Name the blood parasite species.
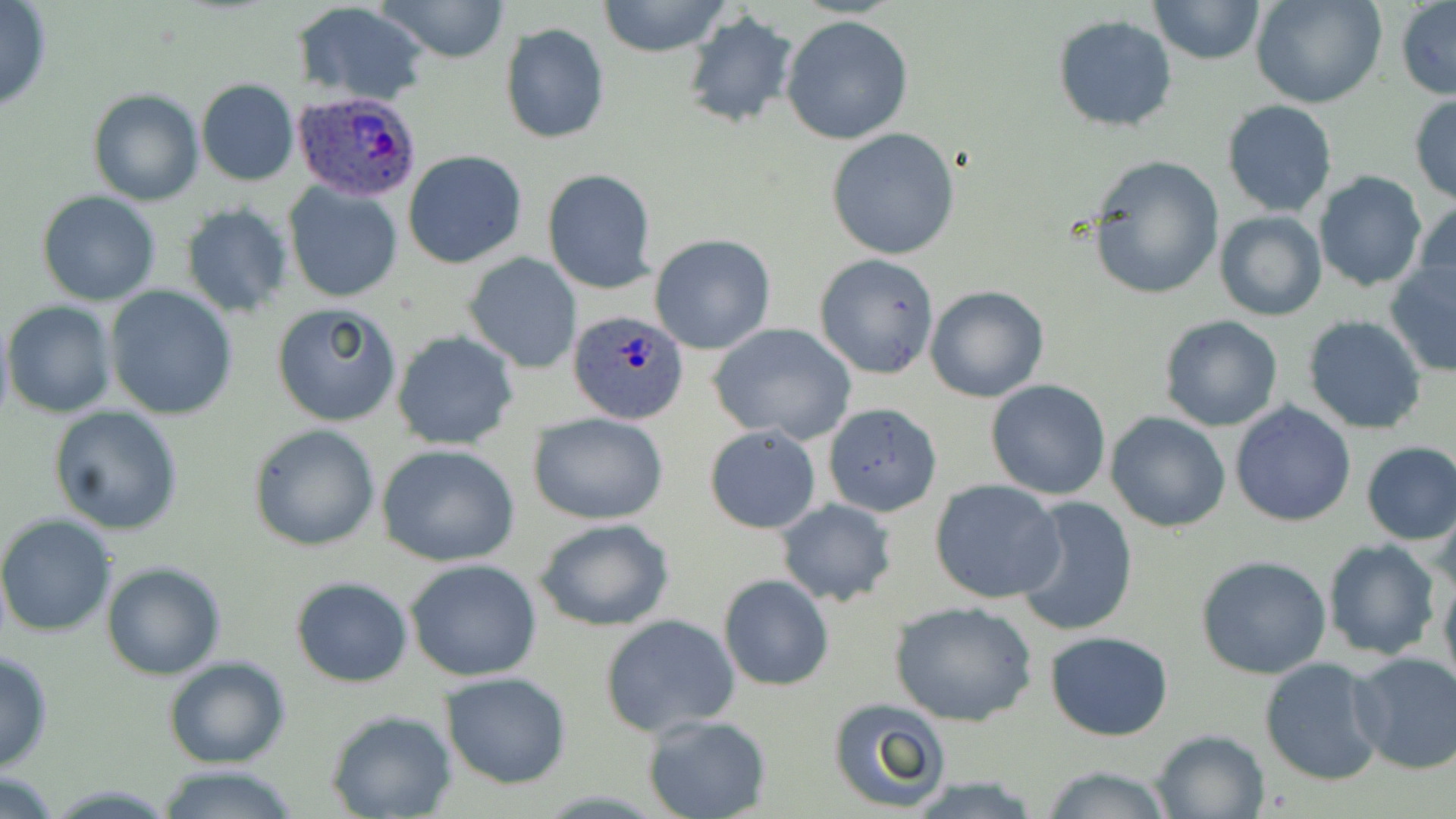

Plasmodium ovale.

Summary:
  - Coordinate format: approximate bounding boxes as [x1, y1, x2, y2] in pixels
  - Uninfected red blood cell locations: [0, 0, 51, 110], [379, 0, 512, 63], [597, 0, 732, 57], [1148, 0, 1267, 66], [1252, 0, 1387, 108], [1396, 1, 1456, 101], [292, 2, 430, 105], [682, 12, 797, 128], [781, 15, 914, 144], [1052, 15, 1178, 134], [499, 23, 610, 145], [197, 78, 300, 186], [88, 90, 203, 206], [1408, 92, 1456, 203], [1221, 100, 1337, 218], [827, 127, 960, 259], [403, 150, 528, 269], [1086, 155, 1224, 301], [543, 169, 658, 294], [1313, 170, 1427, 293], [283, 181, 404, 303], [38, 192, 163, 307], [1414, 201, 1456, 305], [180, 205, 293, 318], [1215, 210, 1327, 321], [650, 235, 776, 355], [464, 252, 581, 373], [814, 254, 940, 379], [1384, 258, 1456, 380], [925, 284, 1049, 403], [105, 287, 237, 420], [3, 302, 118, 418], [271, 303, 403, 427], [1158, 314, 1284, 431], [1302, 315, 1428, 434], [709, 322, 857, 443], [392, 330, 519, 451], [984, 379, 1111, 500], [1230, 401, 1357, 527], [822, 402, 943, 517], [49, 405, 184, 534], [1106, 411, 1231, 532], [528, 413, 670, 525], [248, 423, 381, 551], [703, 424, 821, 534], [1360, 441, 1456, 545], [377, 444, 522, 567], [930, 480, 1067, 604], [1011, 496, 1139, 636], [1434, 499, 1456, 600], [775, 500, 896, 607], [0, 515, 117, 639], [532, 517, 676, 633], [1323, 540, 1441, 660], [1195, 554, 1332, 679], [404, 559, 545, 682], [101, 562, 227, 680], [1439, 567, 1456, 700], [719, 574, 833, 690], [289, 576, 413, 687], [888, 599, 1038, 726], [600, 614, 741, 738], [1046, 631, 1173, 741], [0, 650, 52, 772], [1349, 652, 1456, 776], [162, 655, 291, 769], [1259, 656, 1386, 785], [440, 672, 572, 789], [826, 697, 951, 813], [325, 710, 456, 819], [643, 714, 772, 819], [1150, 728, 1272, 818], [1038, 763, 1177, 819], [154, 765, 299, 819], [0, 770, 62, 818]
  - Plasmodium ovale-infected red blood cell locations: [291, 88, 423, 200], [569, 309, 691, 424]
  - Modality: light microscopy
  - Image size: 1456×819 pixels
  - Magnification: 1000x
  - Preparation: thin blood smear
  - Field of view: one of a larger specimen
  - Stain: May-Grünwald-Giemsa